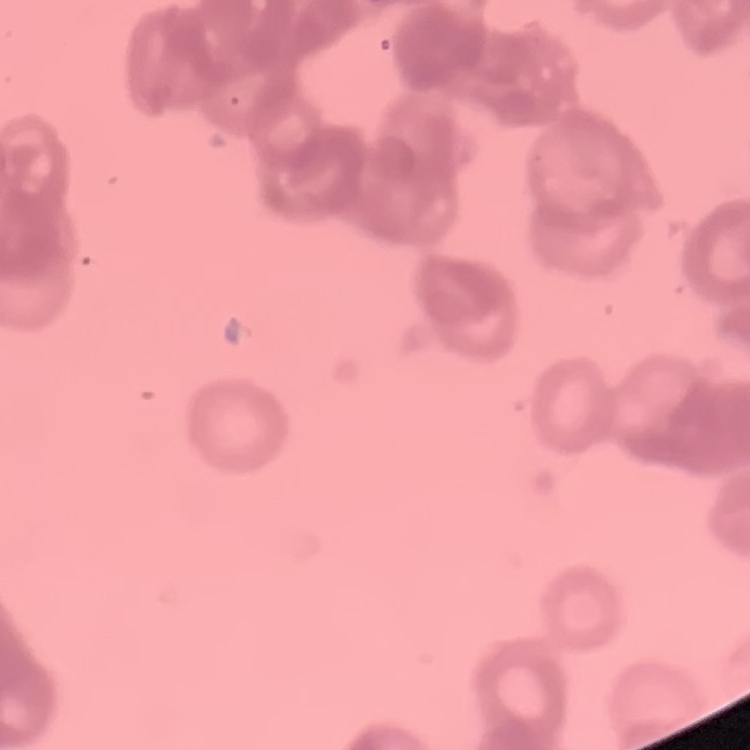

erythrocyte morphology = rouleaux formation
stain = Field's or Giemsa
image type = square crop of a larger photomicrograph
preparation = thin blood smear